State which cell type is depicted.
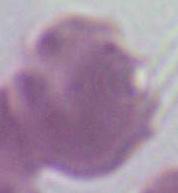

This is an erythrocyte.

Summary:
  - Modality: micrograph
  - Magnification: 1000x